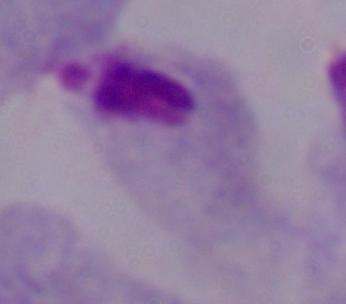
A trichomonad is seen. Captured at 1000x magnification. Photomicrograph.